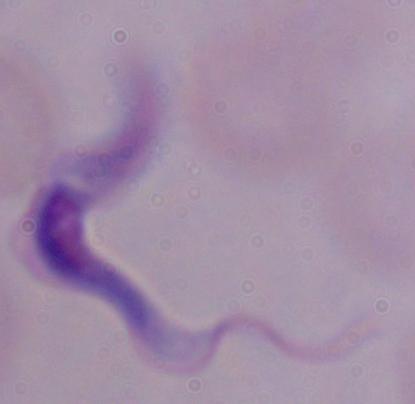
Summary:
  - Identification: trypanosome
  - Modality: photomicrograph
  - Magnification: 1000x